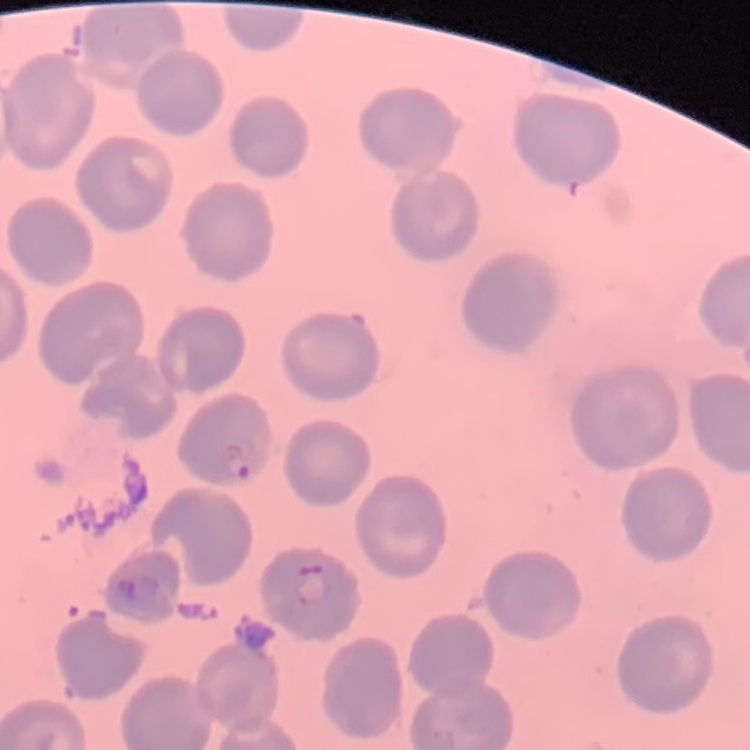
erythrocyte morphology = no rouleaux formation
stain = Field's or Giemsa
preparation = thin peripheral smear
image type = one tile cut from a larger photomicrograph